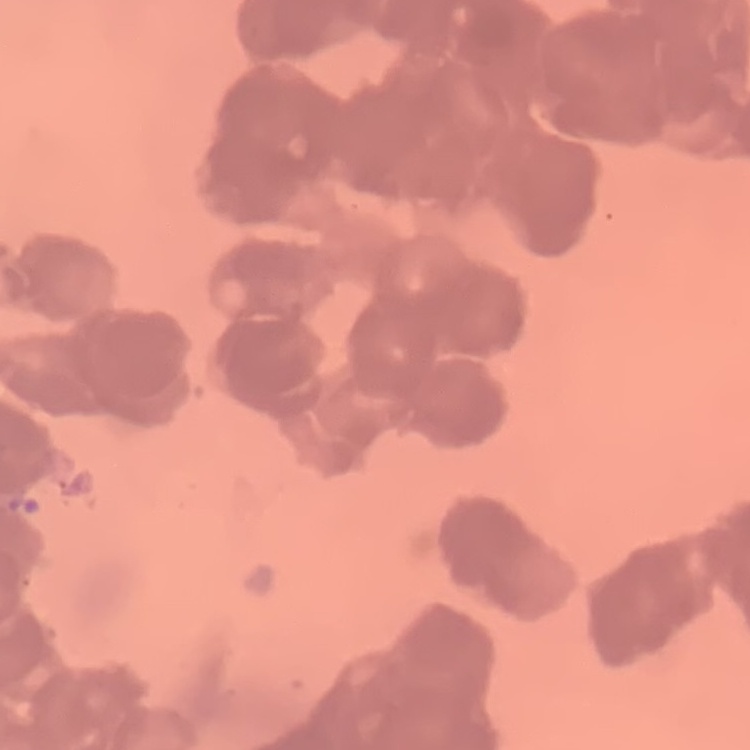
{
  "erythrocyte_morphology": "rouleaux formation",
  "image_type": "one tile cut from a larger photomicrograph",
  "preparation": "thin peripheral smear",
  "stain": "Field's or Giemsa"
}